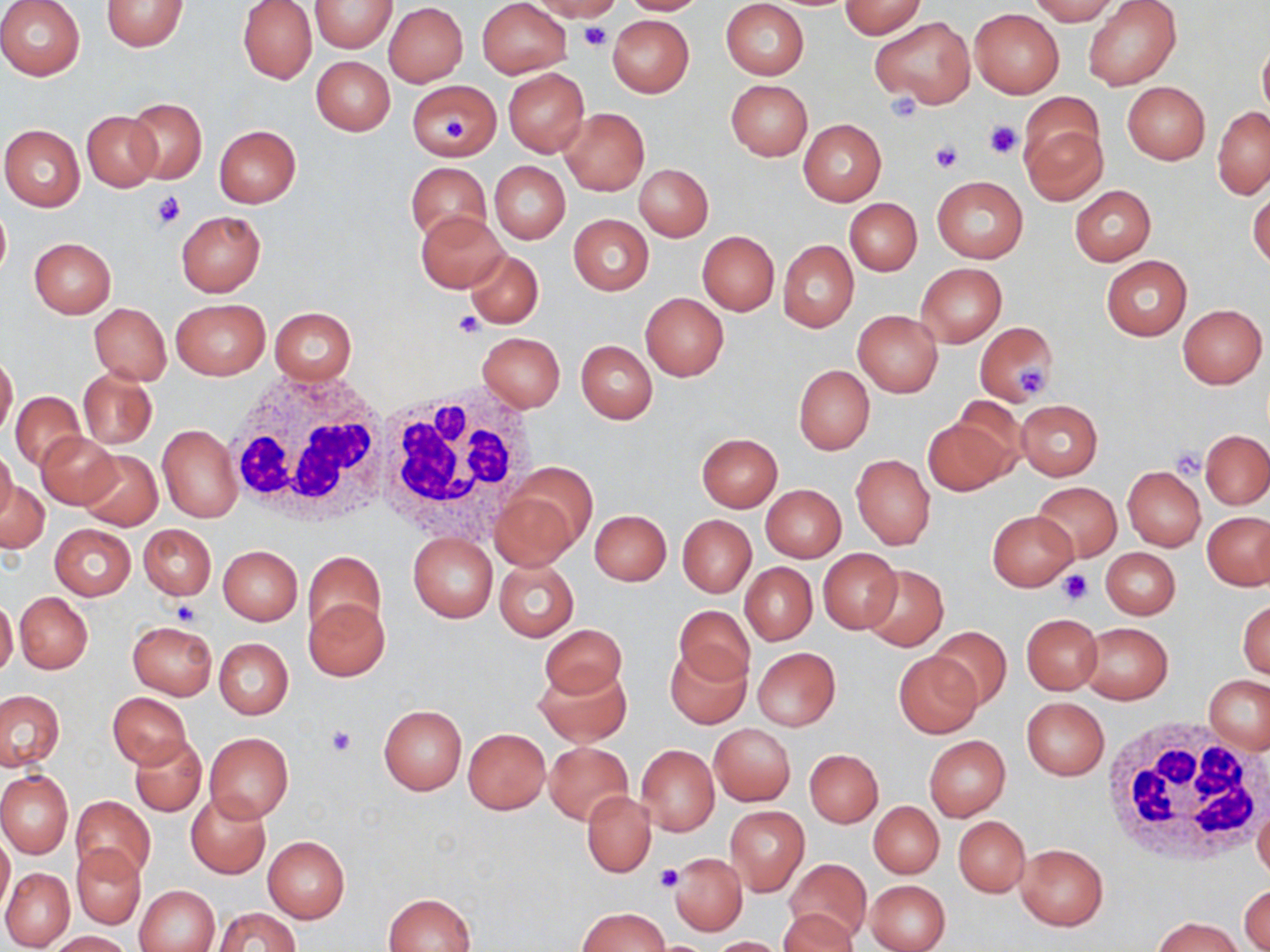 Approximate bounding boxes as [x1, y1, x2, y2] in pixels. Platelet locations: [579, 22, 612, 52], [885, 93, 922, 125], [443, 117, 471, 140], [985, 119, 1020, 160], [932, 142, 962, 171], [153, 189, 187, 232], [454, 311, 486, 338], [1016, 365, 1049, 392], [1170, 447, 1207, 478], [1060, 569, 1092, 603], [171, 600, 203, 625], [325, 726, 356, 756], [654, 863, 685, 891]. Uninfected red blood cell locations: [0, 0, 86, 80], [101, 0, 189, 52], [309, 0, 397, 51], [477, 0, 572, 78], [528, 0, 622, 21], [617, 0, 708, 15], [721, 0, 809, 80], [1026, 0, 1119, 24], [237, 1, 317, 85], [838, 1, 927, 38], [1083, 1, 1182, 89], [383, 3, 469, 87], [969, 8, 1064, 97], [553, 14, 620, 44], [607, 15, 695, 97], [871, 17, 974, 106], [1258, 38, 1270, 120], [312, 56, 394, 135], [503, 68, 589, 157], [725, 79, 811, 160], [408, 80, 501, 160], [1122, 82, 1210, 165], [125, 98, 207, 184], [1212, 106, 1270, 197], [559, 108, 649, 196], [81, 111, 162, 191], [1021, 117, 1107, 205], [799, 119, 886, 205], [0, 124, 86, 211], [214, 124, 301, 207], [490, 161, 570, 244], [406, 162, 490, 245], [634, 163, 713, 241], [931, 175, 1028, 262], [1070, 185, 1155, 266], [1248, 189, 1269, 270], [846, 198, 922, 275], [0, 204, 11, 279], [416, 210, 508, 292], [175, 211, 266, 296], [568, 214, 653, 294], [697, 231, 779, 316], [29, 238, 115, 318], [779, 240, 859, 332], [465, 250, 542, 327], [1102, 256, 1191, 340], [916, 263, 1007, 347], [640, 292, 728, 381], [170, 298, 269, 379], [90, 303, 170, 384], [1178, 304, 1267, 389], [269, 306, 357, 384], [853, 310, 943, 396], [974, 322, 1058, 406], [477, 331, 566, 411], [576, 340, 657, 423], [0, 353, 18, 439], [793, 365, 874, 454], [77, 368, 157, 449], [10, 391, 84, 471], [1014, 400, 1102, 480], [923, 415, 1015, 496], [157, 425, 242, 522], [1201, 429, 1269, 509], [36, 432, 122, 508], [696, 433, 782, 511], [0, 449, 17, 522], [77, 450, 162, 531], [852, 455, 935, 549], [1123, 466, 1206, 550], [494, 468, 591, 566], [1, 481, 50, 555], [1033, 483, 1121, 561], [760, 484, 846, 563], [579, 505, 661, 642], [591, 510, 671, 584], [987, 510, 1078, 591], [1203, 511, 1270, 590], [678, 515, 756, 597], [139, 523, 216, 600], [50, 524, 135, 599], [408, 533, 497, 622], [218, 545, 303, 626], [1100, 547, 1179, 619], [818, 548, 902, 634], [302, 551, 388, 643], [494, 558, 579, 641], [740, 563, 817, 643], [860, 564, 948, 652], [15, 592, 93, 673], [0, 598, 18, 678], [305, 598, 390, 680], [1238, 600, 1270, 679], [673, 605, 755, 689], [1021, 614, 1103, 695], [127, 621, 217, 700], [1078, 622, 1173, 704], [541, 624, 627, 702], [931, 626, 1011, 709], [214, 638, 293, 719], [665, 646, 751, 728], [752, 647, 840, 730], [895, 651, 983, 738], [535, 664, 631, 745], [1204, 676, 1270, 753], [1, 691, 63, 770], [107, 692, 192, 769], [1021, 697, 1110, 780], [378, 704, 467, 795], [710, 723, 795, 805], [462, 728, 550, 815], [205, 732, 294, 821], [130, 735, 206, 818], [924, 735, 1010, 820], [544, 741, 633, 824], [636, 744, 719, 835], [805, 749, 883, 827], [0, 770, 73, 857], [582, 790, 655, 877], [185, 792, 270, 878], [71, 795, 155, 881], [1253, 799, 1270, 886], [869, 800, 944, 878], [725, 806, 808, 895], [953, 816, 1029, 896], [1, 831, 13, 917], [262, 835, 350, 923], [1015, 844, 1109, 930], [71, 845, 144, 929], [670, 853, 747, 935], [785, 859, 872, 944], [1, 867, 73, 950], [867, 879, 950, 952], [136, 886, 219, 952], [1239, 886, 1269, 952], [385, 892, 476, 952], [214, 906, 301, 951], [576, 907, 670, 952], [779, 908, 860, 952], [1151, 916, 1248, 952], [46, 931, 134, 951], [706, 936, 791, 952]. White blood cell locations: [228, 371, 394, 525], [372, 384, 534, 539], [1097, 717, 1270, 864]. Slide-level diagnosis: no evidence of blood parasites. Image is 1270×952 pixels. Optical microscopy. Single field of view. May-Grünwald-Giemsa-stained preparation. Captured at 1000x magnification. Thin blood smear.